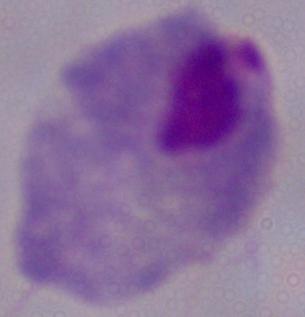

modality = photomicrograph
identification = trichomonad
magnification = 1000x